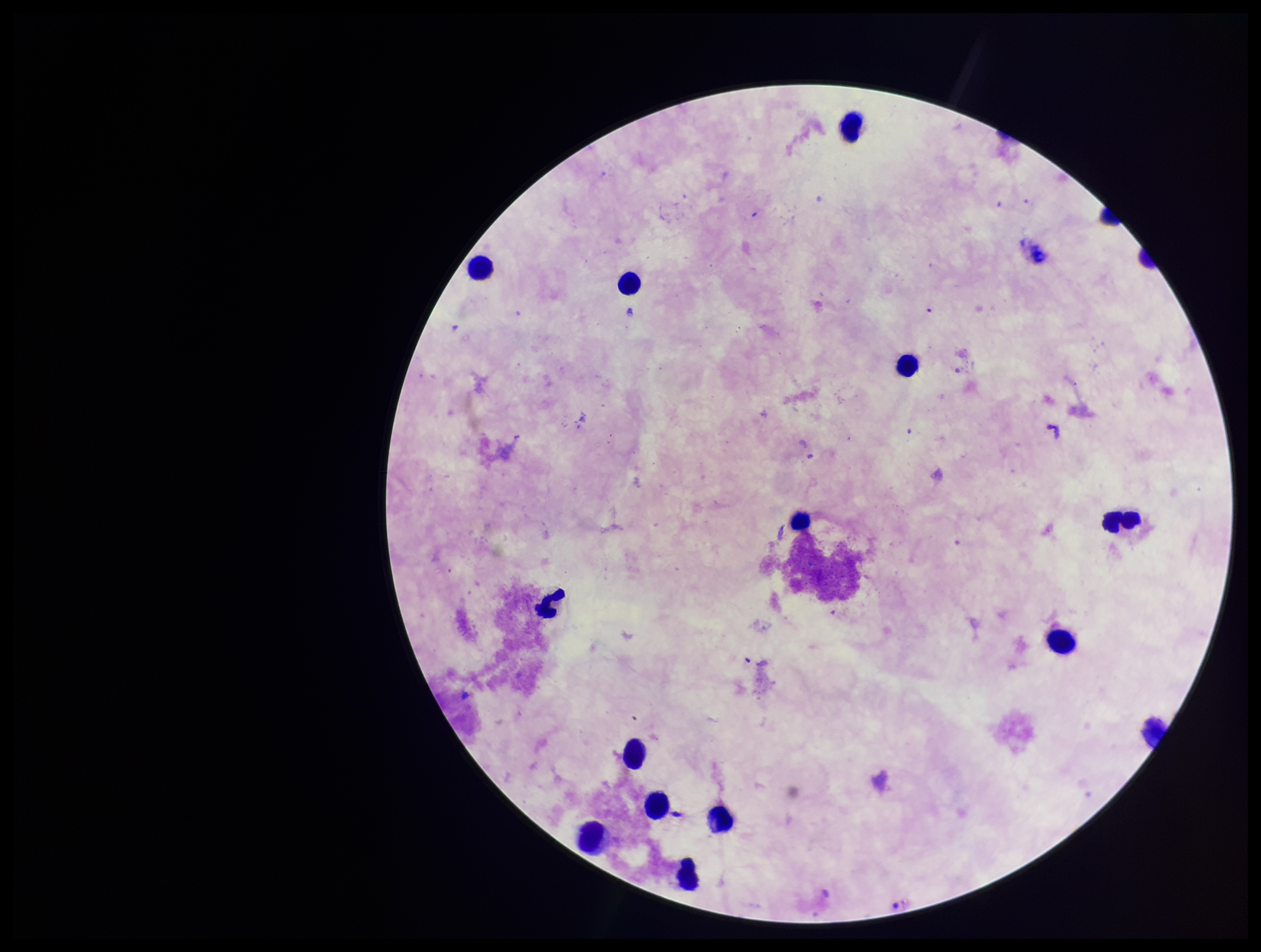
Summary:
  - Field of view: one from this slide
  - Capture: smartphone photograph through the microscope eyepiece
  - Stain: Giemsa
  - Preparation: thick
  - Parasite count: 0
  - Image size: 1261×952 pixels
  - Leukocyte count: 15
  - Plasmodium parasites: none identified
  - Patient malaria status: negative